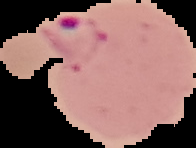

Image is 196×148 pixels. Malaria status: parasitized. From a thin blood smear. Segmented cell region on a black background.